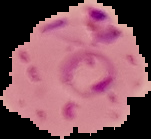
{
  "preparation": "thin blood film",
  "result": "Plasmodium parasites identified",
  "image_type": "cell region segmented out of the field of view; surrounding area masked to black",
  "image_size": "151×139 pixels"
}